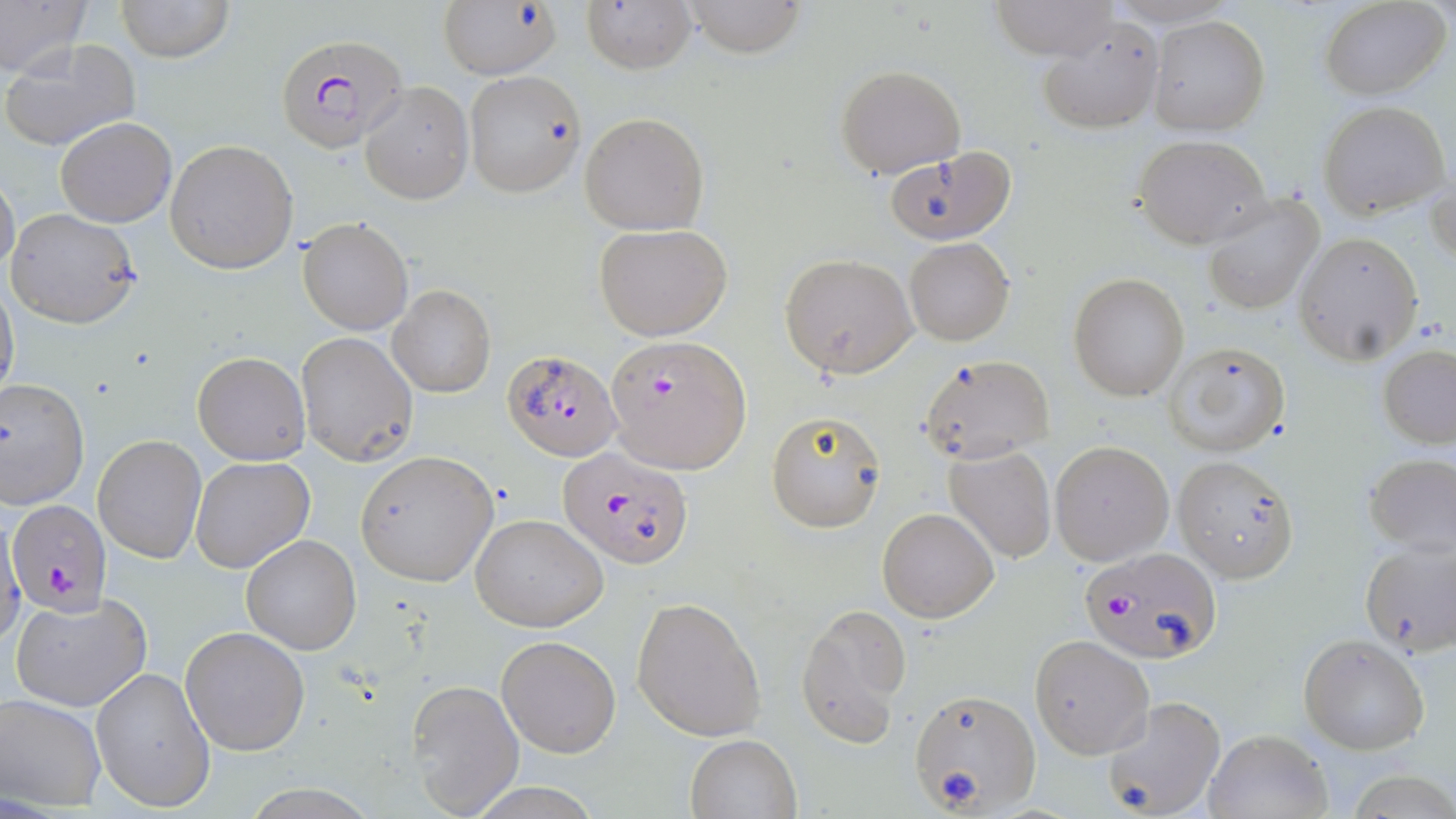
Summary:
  - Coordinate format: approximate bounding boxes as [x1, y1, x2, y2] in pixels
  - Uninfected red blood cell locations: [0, 0, 92, 82], [117, 0, 233, 64], [440, 0, 563, 79], [582, 0, 698, 73], [682, 0, 806, 56], [990, 0, 1120, 61], [1320, 0, 1451, 100], [1102, 2, 1245, 27], [1148, 15, 1270, 135], [1040, 19, 1165, 133], [2, 38, 141, 152], [836, 65, 966, 178], [464, 70, 586, 198], [360, 81, 474, 204], [1319, 101, 1449, 218], [578, 110, 710, 235], [55, 118, 176, 227], [1134, 136, 1270, 246], [165, 139, 297, 273], [884, 145, 1018, 246], [1428, 160, 1456, 273], [0, 169, 20, 278], [1201, 195, 1325, 316], [6, 207, 144, 330], [298, 217, 414, 335], [594, 222, 734, 340], [1295, 233, 1423, 362], [904, 237, 1014, 345], [779, 253, 916, 377], [1068, 273, 1189, 400], [0, 281, 19, 404], [387, 284, 496, 399], [296, 332, 419, 466], [1164, 340, 1292, 457], [1378, 345, 1456, 448], [191, 351, 310, 464], [916, 353, 1057, 463], [0, 378, 90, 509], [765, 410, 886, 532], [94, 435, 206, 564], [1050, 440, 1173, 565], [943, 444, 1058, 564], [354, 450, 499, 586], [1364, 452, 1455, 556], [189, 456, 314, 575], [1173, 457, 1301, 581], [877, 508, 998, 622], [469, 512, 608, 632], [0, 518, 26, 653], [241, 534, 362, 656], [1358, 539, 1456, 657], [10, 593, 152, 714], [631, 597, 767, 742], [795, 603, 913, 748], [180, 626, 312, 756], [496, 635, 620, 758], [1030, 635, 1154, 758], [1299, 635, 1430, 754], [91, 667, 216, 813], [407, 679, 525, 818], [908, 687, 1041, 815], [0, 694, 107, 811], [1098, 695, 1227, 819], [1204, 726, 1333, 818], [685, 734, 800, 818], [1347, 771, 1456, 817]
  - Plasmodium falciparum-infected red blood cell locations: [275, 33, 407, 154], [606, 335, 751, 472], [500, 348, 622, 460], [559, 447, 697, 569], [8, 498, 112, 615], [1080, 549, 1221, 664]
  - Slide-level diagnosis: Plasmodium falciparum
  - Stain: May-Grünwald-Giemsa
  - Magnification: 1000x
  - Modality: optical microscopy
  - Field of view: one of a larger specimen
  - Preparation: thin blood smear
  - Image size: 1456×819 pixels